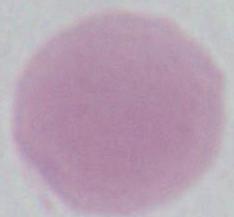 Micrograph. 1000x magnification. A red blood cell is shown.